Assess the morphology of the red blood cells.
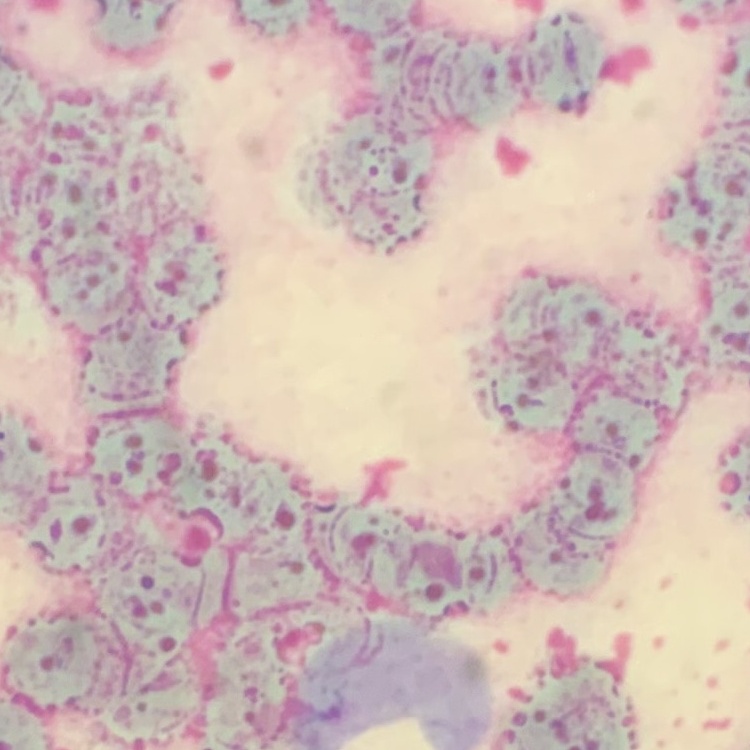

Rouleaux formation.

Summary:
  - Image type: square crop of a larger photomicrograph
  - Stain: Field's or Giemsa
  - Preparation: thin blood film